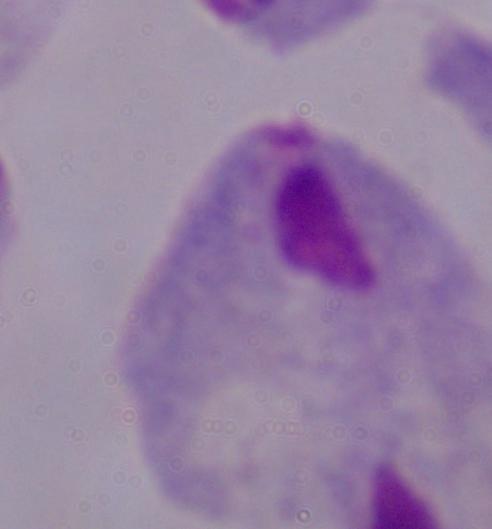
Summary:
  - Modality: micrograph
  - Magnification: 1000x
  - Identification: trichomonad